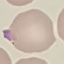
Result: malaria parasites detected. Thin blood film. Cell patch, automatically extracted from a larger field of view and resized to 64 × 64 pixels. Giemsa stain. Photographed with a smartphone camera at the microscope eyepiece.